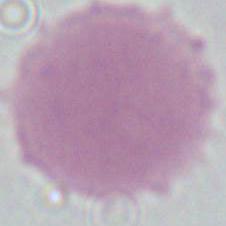 Photomicrograph. Captured at 1000x magnification. An erythrocyte is shown.